Point out each malaria parasite.
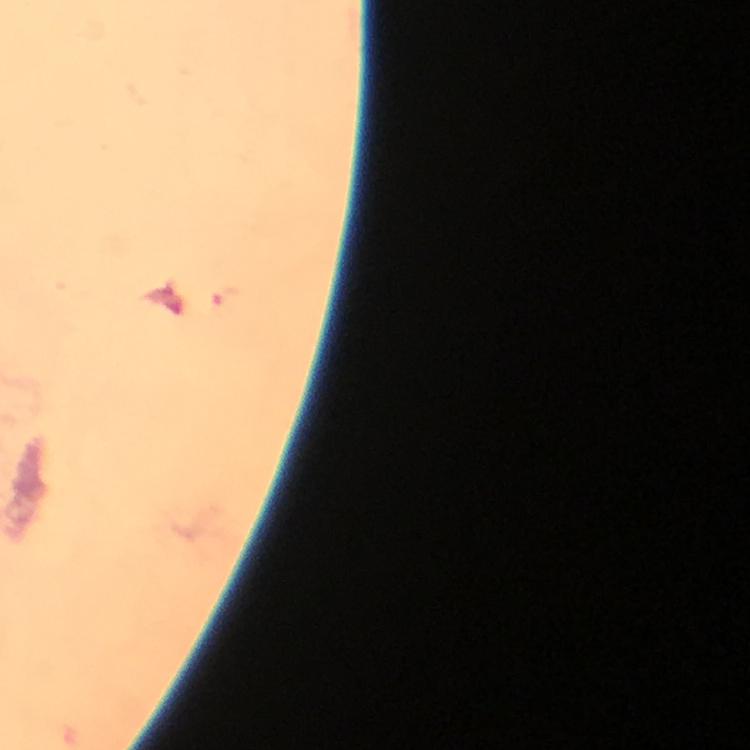

Approximate centers as {x, y} in pixels.
Malaria parasites: {223, 298}.

A crop from one field of view. Immersion oil applied. Thick blood film. Giemsa stain. At 100x magnification. Image is 750×750 pixels. From a diagnostic examination for malaria. Smartphone photograph taken through a microscope.